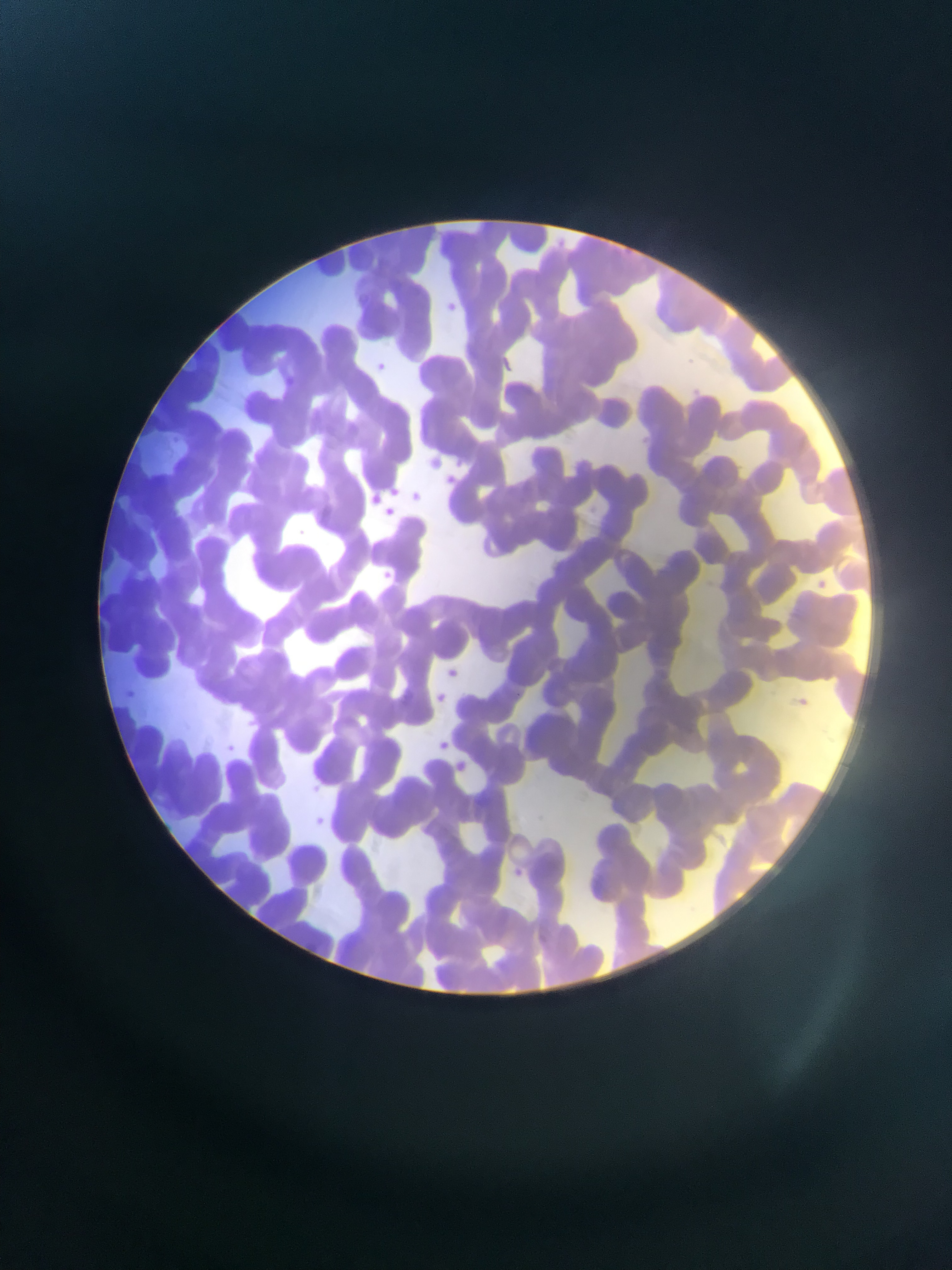
capture = mobile-phone photograph through a microscope
image size = 952×1270 pixels
country = Ghana
preparation = thin blood smear
field of view = single
malaria parasite locations = approximate bounding boxes as (left, top, right, bottom) in pixels: (439, 298, 462, 319), (372, 361, 388, 376), (277, 372, 307, 393), (687, 382, 707, 394), (441, 472, 459, 488), (408, 489, 424, 504), (365, 491, 383, 508), (292, 527, 308, 541), (376, 569, 394, 586), (809, 577, 831, 595), (125, 685, 137, 697), (406, 686, 423, 701), (794, 695, 828, 716), (434, 739, 451, 754), (221, 740, 239, 757), (309, 812, 331, 831), (514, 862, 533, 882)